Comment on the morphology of the erythrocytes.
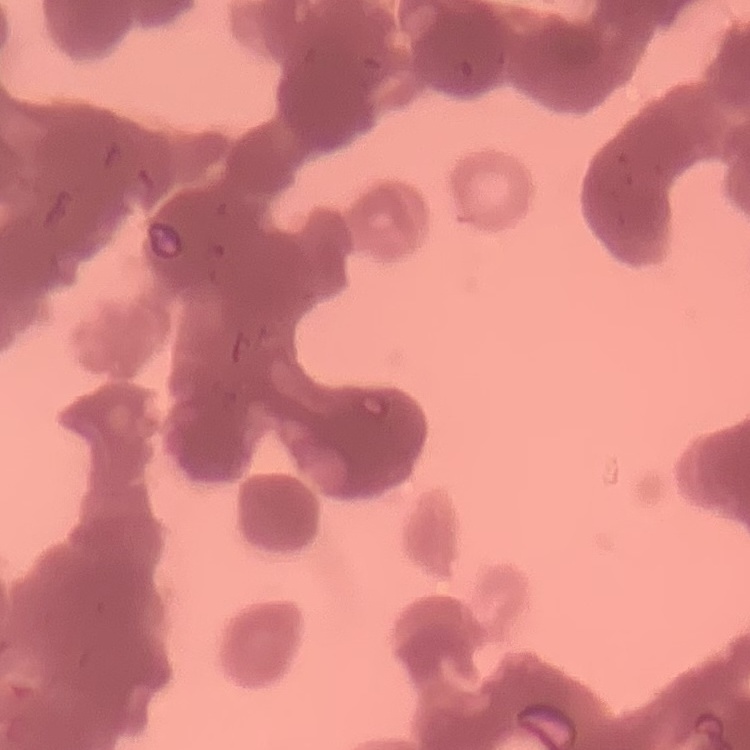
They show rouleaux formation.

stain = Field's or Giemsa
image type = one tile cut from a larger photomicrograph
preparation = thin blood smear